Give the position of every malaria parasite.
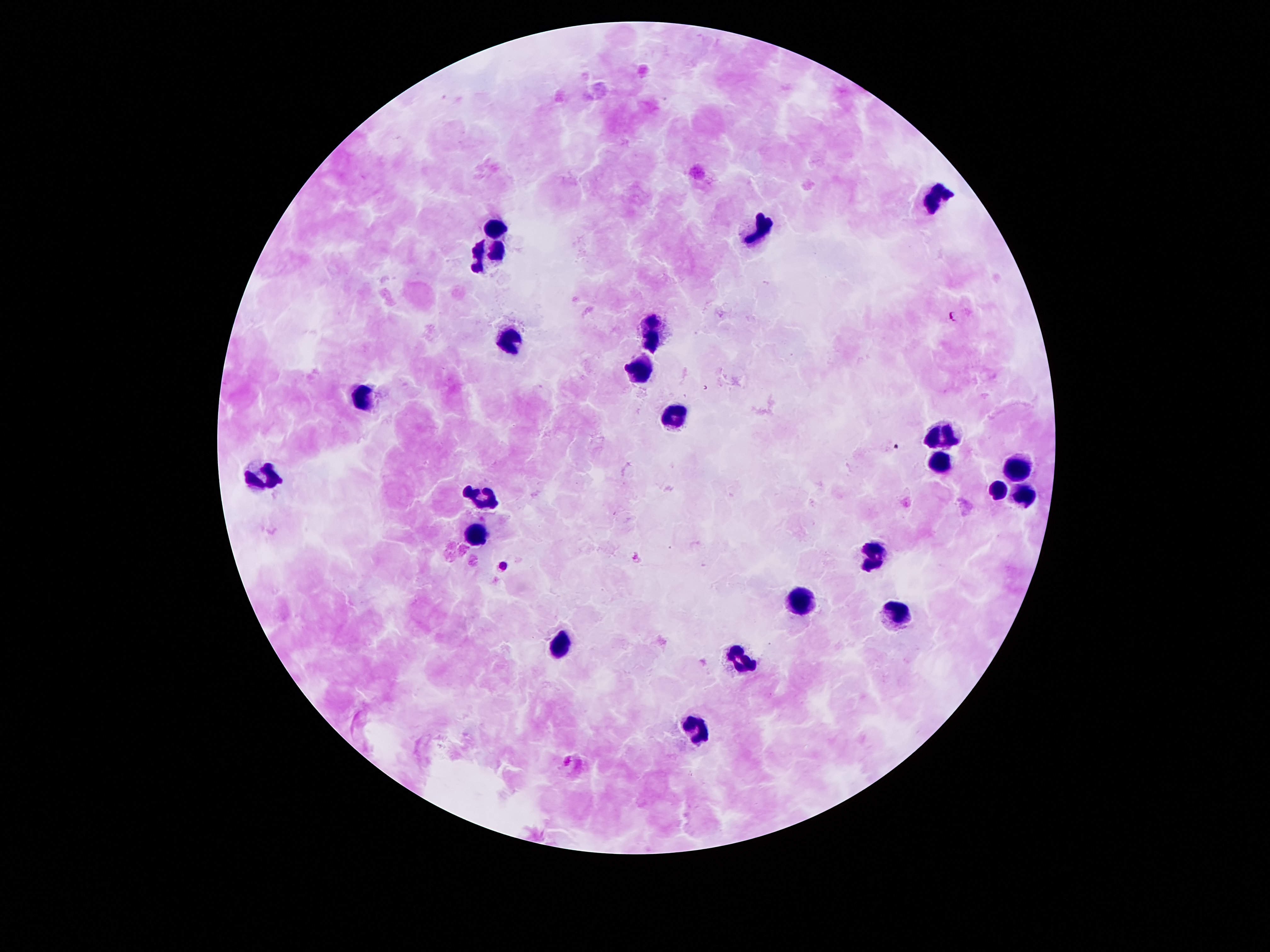

Approximate centers as [x, y] in pixels.
Malaria parasites: [953, 315], [635, 558], [506, 564].

Leukocyte locations: [938, 197], [496, 230], [759, 234], [485, 253], [653, 328], [511, 339], [637, 367], [365, 395], [673, 420], [947, 437], [940, 462], [1013, 468], [264, 477], [998, 489], [1024, 493], [483, 495], [472, 531], [872, 552], [794, 599], [898, 612], [558, 650], [739, 661], [697, 729]. Image is 1270×952 pixels. Thick peripheral-blood smear. 100x magnification. Smartphone photograph taken through the microscope eyepiece. Giemsa stain. Patient malaria status: positive for Plasmodium falciparum. One field from this slide.